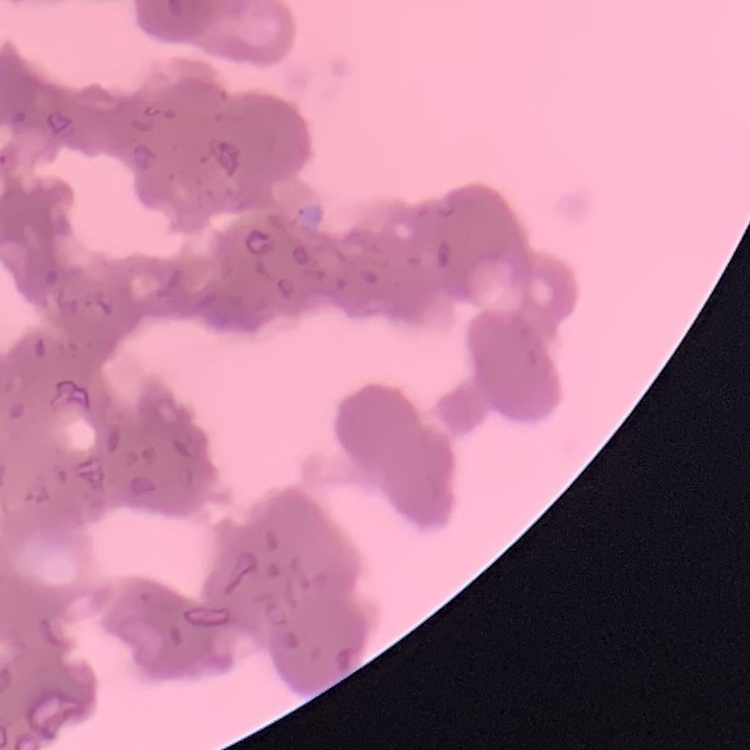

The erythrocytes show rouleaux formation. Field's or Giemsa stain. Square crop of a larger photomicrograph. Thin blood smear.